Outline each blood parasite and name the species.
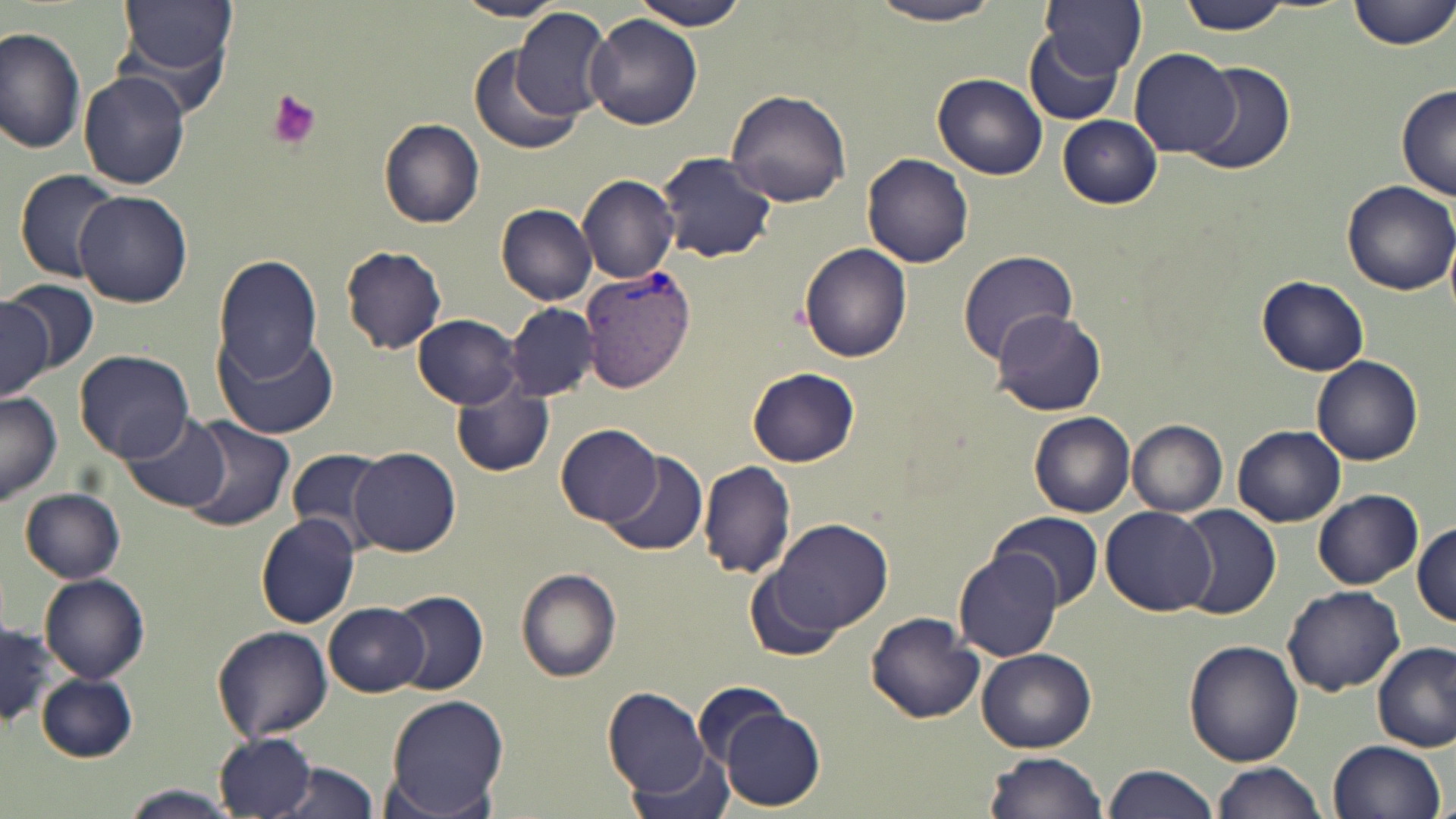

Approximate bounding boxes as named x1/y1/x2/y2 corners in pixels.
Plasmodium vivax-infected red blood cells: (x1=578, y1=264, x2=695, y2=394).
No Plasmodium falciparum, Plasmodium ovale, Plasmodium malariae, Babesia divergens, or Trypanosoma brucei observed.

{
  "slide_level_diagnosis": "Plasmodium vivax",
  "preparation": "thin blood smear",
  "platelet_locations": "approximate bounding boxes as named x1/y1/x2/y2 corners in pixels: (x1=266, y1=91, x2=323, y2=150)",
  "field_of_view": "single",
  "modality": "light microscopy",
  "uninfected_red_blood_cell_locations": "approximate bounding boxes as named x1/y1/x2/y2 corners in pixels: (x1=118, y1=0, x2=239, y2=83), (x1=453, y1=0, x2=571, y2=21), (x1=632, y1=0, x2=749, y2=29), (x1=1040, y1=0, x2=1147, y2=77), (x1=1176, y1=0, x2=1297, y2=35), (x1=1350, y1=0, x2=1454, y2=51), (x1=867, y1=1, x2=1010, y2=27), (x1=511, y1=7, x2=613, y2=120), (x1=586, y1=14, x2=703, y2=130), (x1=113, y1=25, x2=235, y2=122), (x1=1, y1=27, x2=85, y2=157), (x1=1024, y1=31, x2=1124, y2=125), (x1=466, y1=45, x2=583, y2=157), (x1=1131, y1=47, x2=1240, y2=158), (x1=1192, y1=61, x2=1295, y2=176), (x1=79, y1=72, x2=190, y2=190), (x1=932, y1=73, x2=1048, y2=181), (x1=1395, y1=84, x2=1456, y2=202), (x1=725, y1=87, x2=853, y2=208), (x1=1057, y1=114, x2=1163, y2=208), (x1=379, y1=118, x2=485, y2=229), (x1=657, y1=151, x2=777, y2=264), (x1=862, y1=153, x2=973, y2=270), (x1=14, y1=169, x2=120, y2=284), (x1=577, y1=174, x2=680, y2=286), (x1=1339, y1=179, x2=1455, y2=296), (x1=73, y1=191, x2=192, y2=308), (x1=496, y1=203, x2=599, y2=306), (x1=799, y1=244, x2=913, y2=363), (x1=339, y1=246, x2=446, y2=355), (x1=956, y1=249, x2=1082, y2=364), (x1=211, y1=257, x2=323, y2=385), (x1=1257, y1=275, x2=1369, y2=377), (x1=2, y1=279, x2=99, y2=374), (x1=0, y1=296, x2=53, y2=399), (x1=505, y1=302, x2=598, y2=403), (x1=991, y1=310, x2=1107, y2=416), (x1=414, y1=314, x2=522, y2=408), (x1=218, y1=329, x2=339, y2=438), (x1=73, y1=350, x2=196, y2=462), (x1=1313, y1=356, x2=1423, y2=466), (x1=746, y1=367, x2=860, y2=467), (x1=451, y1=383, x2=553, y2=477), (x1=0, y1=392, x2=61, y2=503), (x1=120, y1=411, x2=231, y2=511), (x1=1029, y1=412, x2=1135, y2=517), (x1=180, y1=416, x2=296, y2=534), (x1=1128, y1=419, x2=1228, y2=517), (x1=557, y1=423, x2=661, y2=525), (x1=1232, y1=424, x2=1345, y2=528), (x1=287, y1=446, x2=394, y2=545), (x1=351, y1=447, x2=461, y2=556), (x1=599, y1=451, x2=709, y2=559), (x1=698, y1=460, x2=797, y2=579), (x1=20, y1=488, x2=126, y2=583), (x1=1314, y1=490, x2=1422, y2=589), (x1=1172, y1=504, x2=1282, y2=619), (x1=1101, y1=505, x2=1215, y2=615), (x1=992, y1=511, x2=1103, y2=609), (x1=256, y1=514, x2=362, y2=628), (x1=770, y1=519, x2=894, y2=637), (x1=1412, y1=521, x2=1456, y2=627), (x1=954, y1=549, x2=1063, y2=662), (x1=516, y1=568, x2=623, y2=683), (x1=745, y1=574, x2=840, y2=659), (x1=40, y1=575, x2=150, y2=685), (x1=1282, y1=584, x2=1404, y2=695), (x1=388, y1=591, x2=489, y2=695), (x1=323, y1=601, x2=430, y2=697), (x1=866, y1=611, x2=985, y2=724), (x1=212, y1=625, x2=332, y2=743), (x1=0, y1=626, x2=58, y2=725), (x1=1184, y1=640, x2=1304, y2=767), (x1=1373, y1=642, x2=1455, y2=751), (x1=977, y1=649, x2=1096, y2=752), (x1=36, y1=673, x2=137, y2=762), (x1=696, y1=682, x2=786, y2=768), (x1=603, y1=687, x2=715, y2=800), (x1=380, y1=694, x2=510, y2=819), (x1=717, y1=708, x2=826, y2=812), (x1=213, y1=730, x2=317, y2=817), (x1=1327, y1=738, x2=1446, y2=819), (x1=625, y1=750, x2=739, y2=819), (x1=983, y1=752, x2=1109, y2=819), (x1=269, y1=762, x2=382, y2=819), (x1=1102, y1=763, x2=1222, y2=819), (x1=1210, y1=763, x2=1327, y2=819), (x1=118, y1=785, x2=240, y2=819)",
  "magnification": "1000x",
  "stain": "May-Grünwald-Giemsa",
  "image_size": "1456×819 pixels"
}